Report the malaria status of this cell.
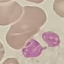
It is uninfected.

Summary:
  - Stain: Giemsa
  - Capture: smartphone camera at the microscope eyepiece
  - Preparation: thin blood smear
  - Image type: cell patch, automatically extracted from a larger field of view and resized to 64 × 64 pixels